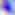

Toxoplasma gondii is shown. Micrograph. Captured at 400x magnification.